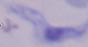

modality: micrograph
identification: trypanosome
magnification: 1000x